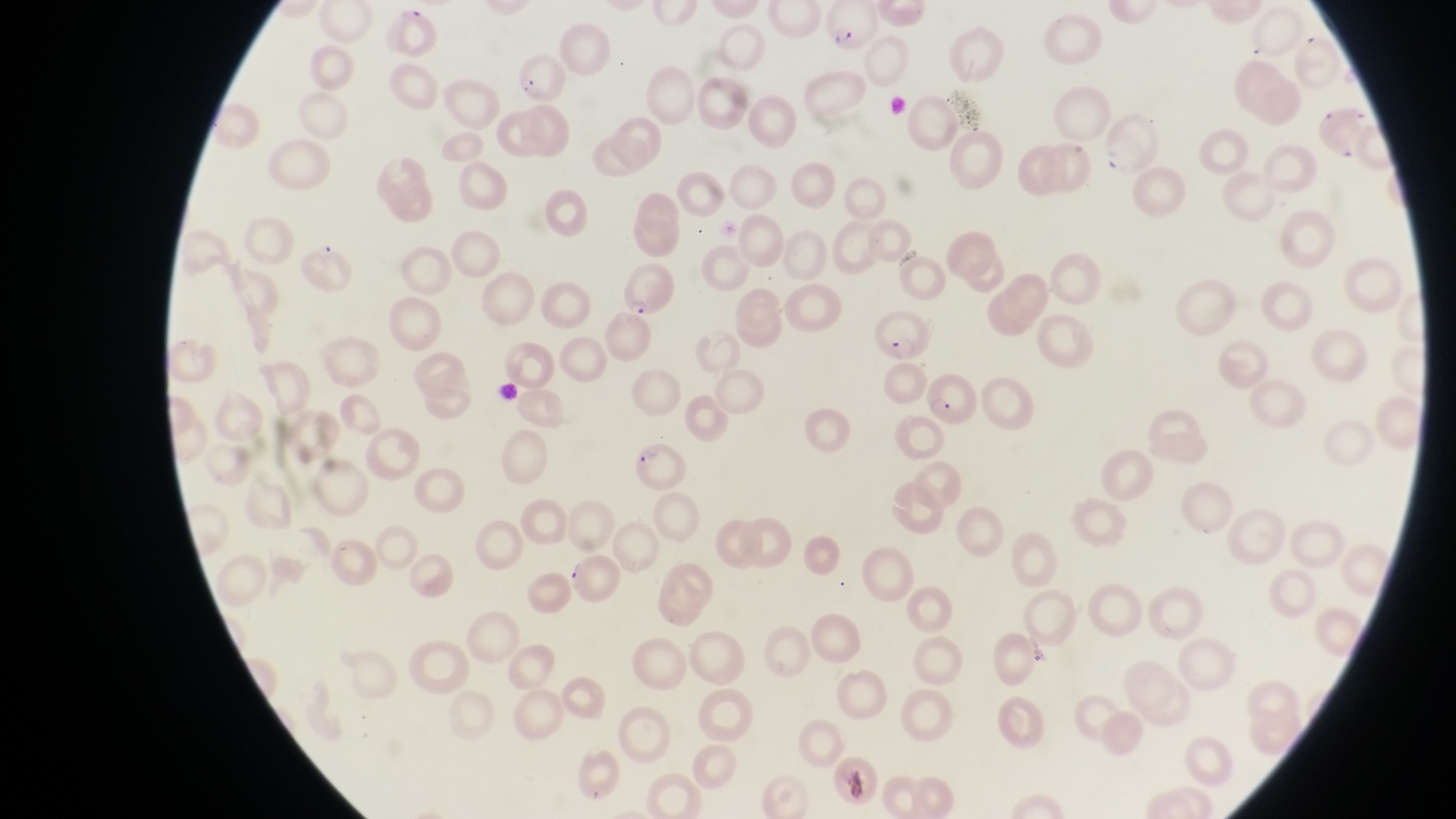
magnification = 1000x
capture = smartphone photograph through the eyepiece of an Olympus CX-23 microscope
preparation = thin blood film
field of view = single
parasitised red blood cell locations = approximate bounding boxes as left top right bottom in pixels: 824 3 880 53; 510 56 579 106; 613 258 677 318; 925 370 978 428; 627 444 694 499; 566 552 626 610
country = Uganda
artifact (platelet-like body, stain precipitate, or debris) locations = approximate bounding boxes as left top right bottom in pixels: 494 377 522 407
image size = 1456×819 pixels